Outline platelets.
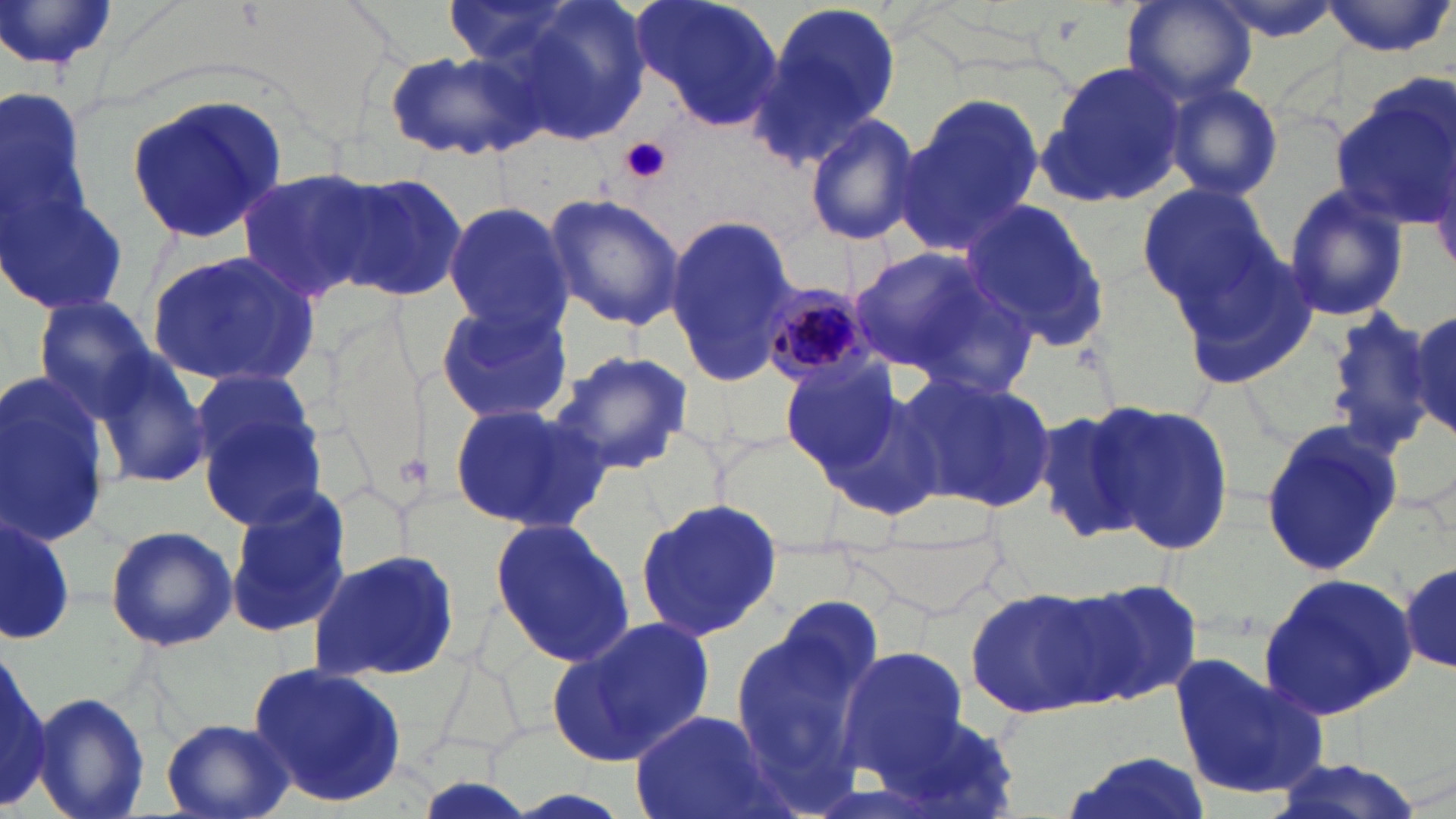
Approximate bounding boxes as (x1,y1)-(x2,y2) corner pairs in pixels.
Platelets: (620,136)-(672,185).

Summary:
  - Plasmodium malariae-infected red blood cell locations: (759,275)-(883,385)
  - Uninfected red blood cell locations: (491,0)-(656,147), (629,0)-(784,133), (1123,0)-(1256,105), (1205,0)-(1346,42), (1321,0)-(1456,57), (750,1)-(903,164), (1,2)-(120,71), (386,48)-(545,164), (1038,61)-(1186,208), (0,74)-(100,268), (1331,76)-(1454,227), (1166,81)-(1286,201), (895,92)-(1047,255), (124,95)-(290,244), (804,113)-(921,246), (240,167)-(380,303), (331,170)-(468,303), (1135,181)-(1276,311), (1280,182)-(1411,324), (1,187)-(133,314), (544,192)-(685,331), (960,195)-(1111,353), (441,203)-(573,333), (662,216)-(802,384), (849,243)-(1000,375), (1174,245)-(1319,388), (145,247)-(323,389), (430,293)-(577,426), (32,294)-(163,419), (1407,308)-(1455,437), (1324,310)-(1440,450), (551,348)-(695,477), (96,352)-(212,487), (779,357)-(908,476), (184,366)-(324,488), (900,371)-(1059,516), (0,374)-(114,552), (817,384)-(945,520), (445,401)-(613,533), (1098,403)-(1236,555), (1031,404)-(1161,544), (198,408)-(329,531), (1259,420)-(1403,581), (223,489)-(352,642), (634,498)-(781,643), (0,511)-(75,647), (489,515)-(634,669), (103,524)-(238,651), (306,547)-(461,682), (1400,558)-(1455,675), (1256,571)-(1420,719), (1069,574)-(1207,707), (964,586)-(1116,722), (731,598)-(883,796), (549,616)-(716,769), (835,646)-(968,784), (1,651)-(51,811), (1169,651)-(1329,801), (248,662)-(408,806), (33,691)-(151,819), (864,706)-(1017,818), (630,710)-(773,819), (159,718)-(296,819), (1062,750)-(1211,819), (1263,759)-(1427,819)
  - Slide-level diagnosis: Plasmodium malariae
  - Modality: light microscopy
  - Preparation: thin blood film
  - Stain: May-Grünwald-Giemsa
  - Field of view: single
  - Image size: 1456×819 pixels
  - Magnification: 1000x